Comment on the morphology of the red blood cells.
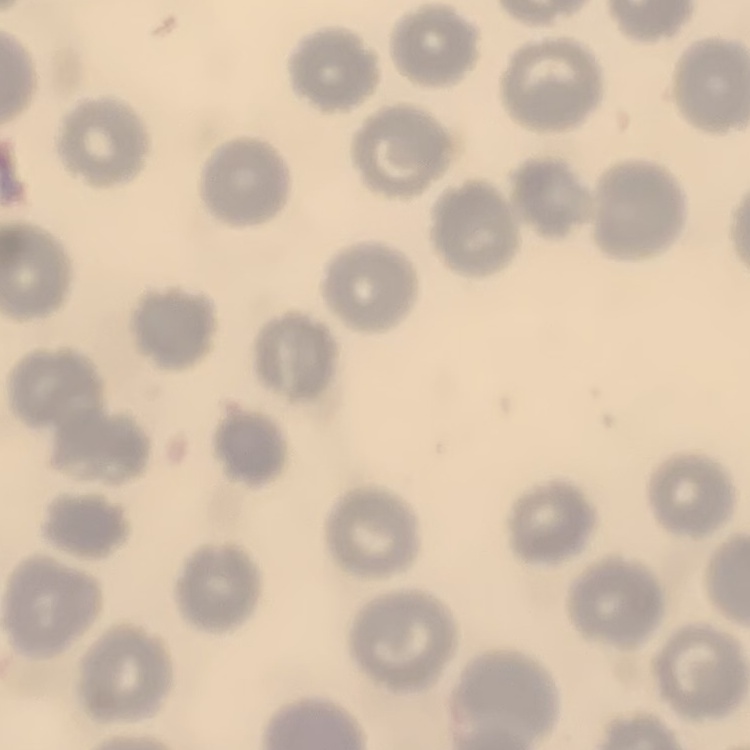
They show no rouleaux formation.

Thin blood film. Stained with either Field's or Giemsa. One tile cut from a larger photomicrograph.